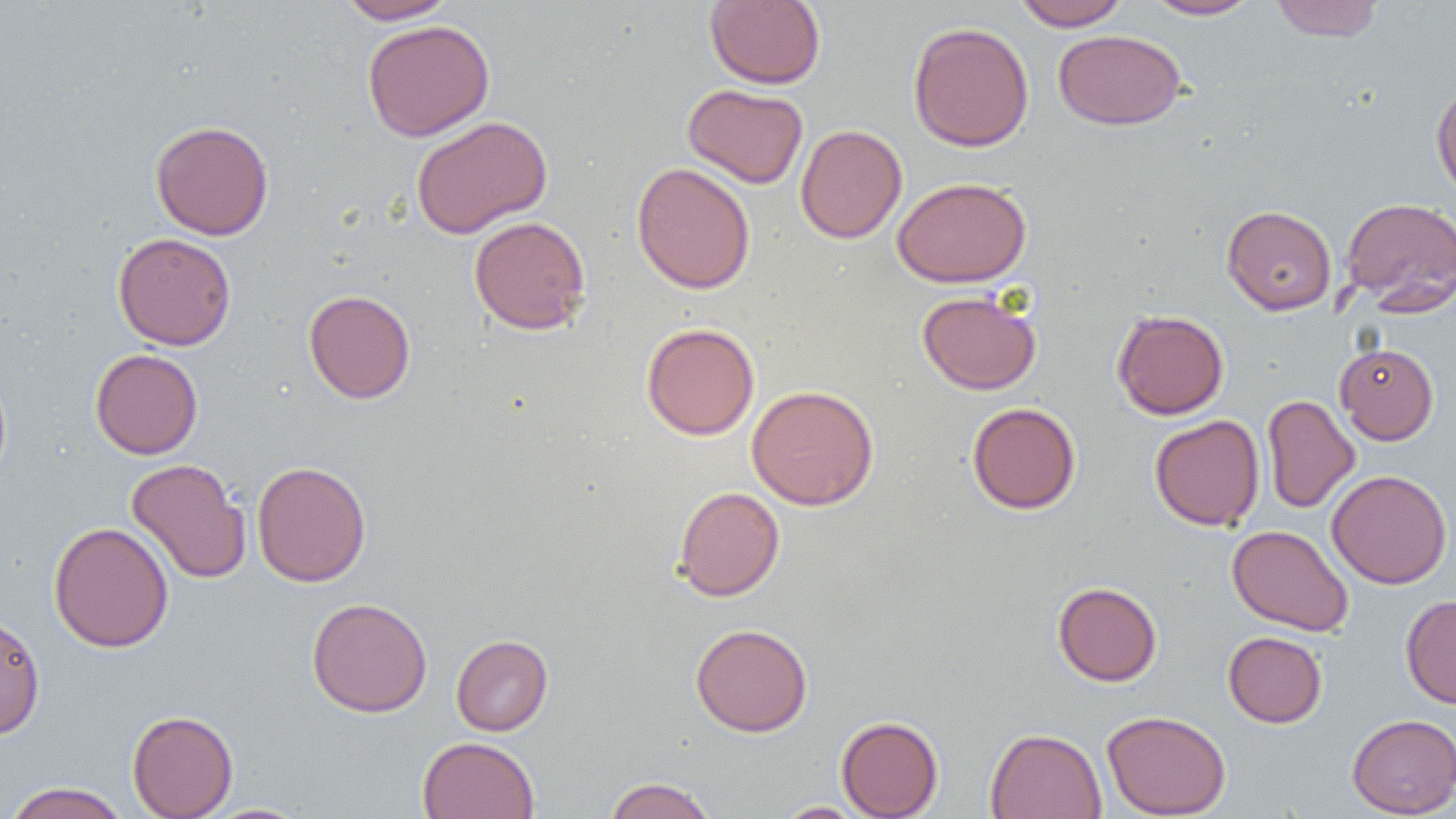

slide_level_diagnosis: no evidence of blood parasites
image_size: 1456×819 pixels
uninfected_red_blood_cell_locations: 'approximate bounding boxes as [x1, y1, x2, y2] in pixels: [335, 0, 458, 24], [705, 0, 826, 89], [1012, 0, 1131, 31], [1143, 0, 1263, 20], [1270, 0, 1384, 42], [362, 19, 495, 142], [908, 21, 1034, 152], [1053, 29, 1186, 130], [1431, 80, 1456, 201], [682, 83, 808, 189], [411, 115, 553, 238], [150, 120, 274, 241], [795, 124, 907, 243], [631, 162, 756, 294], [892, 176, 1031, 288], [1341, 197, 1456, 313], [1221, 204, 1337, 315], [468, 215, 591, 335], [112, 232, 237, 351], [304, 289, 416, 404], [917, 290, 1041, 395], [1112, 309, 1229, 420], [641, 322, 760, 440], [1335, 342, 1439, 445], [90, 348, 203, 459], [0, 369, 12, 488], [746, 384, 879, 510], [1262, 394, 1360, 513], [967, 402, 1081, 514], [1149, 414, 1265, 531], [126, 458, 251, 584], [252, 460, 371, 587], [1326, 469, 1453, 589], [673, 486, 785, 602], [48, 521, 174, 653], [1227, 525, 1354, 636], [1052, 581, 1162, 686], [1400, 594, 1456, 708], [306, 597, 433, 717], [0, 613, 45, 740], [690, 623, 812, 736], [1223, 631, 1327, 728], [451, 634, 553, 736], [127, 709, 238, 819], [1102, 709, 1231, 819], [1346, 713, 1456, 818], [836, 715, 943, 818], [985, 727, 1107, 819], [417, 736, 540, 819], [604, 776, 717, 819], [3, 781, 131, 819], [773, 801, 870, 818], [198, 803, 315, 819]'
magnification: 1000x
modality: optical microscopy
preparation: thin blood film
field_of_view: one of a larger specimen